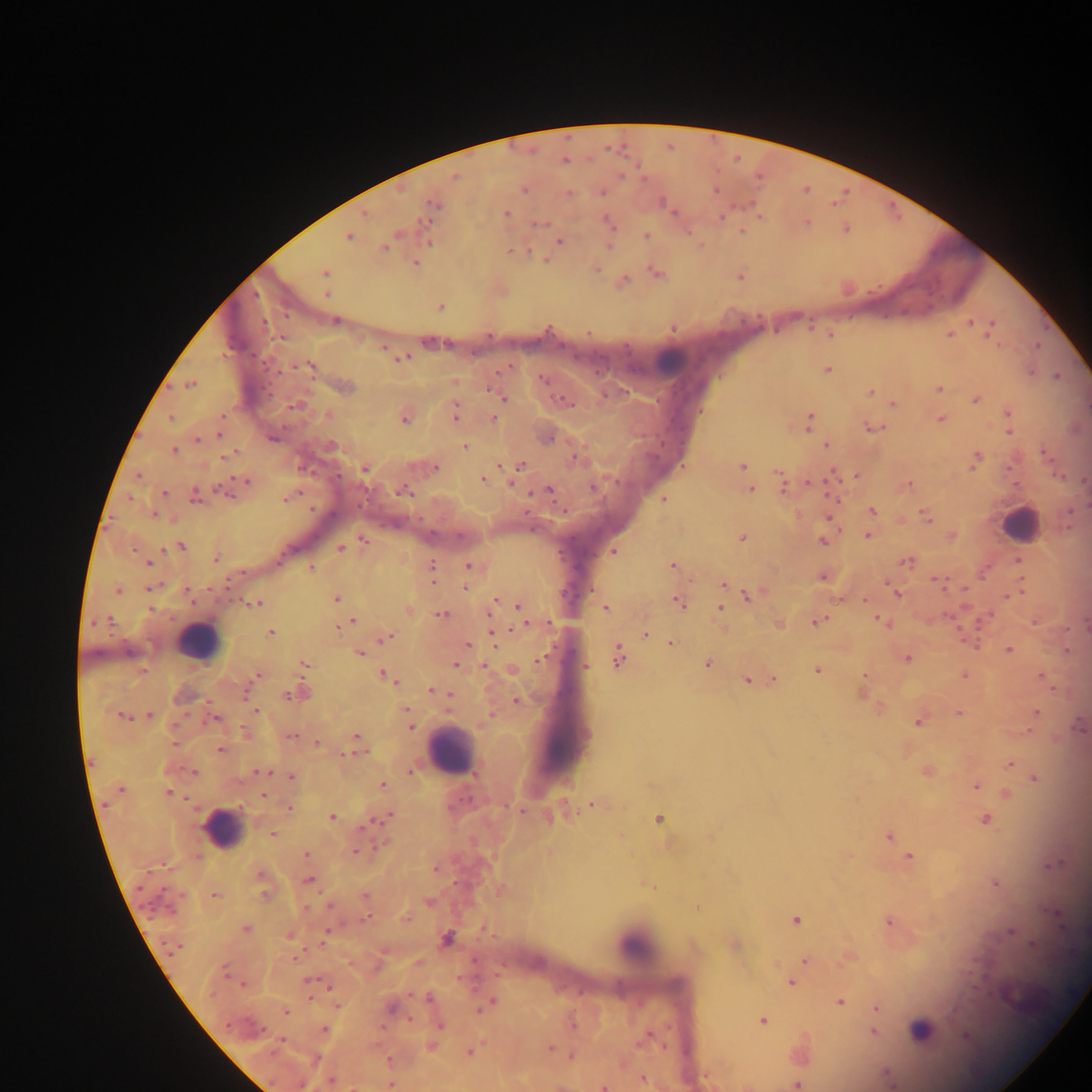
{
  "field_of_view": "single",
  "capture": "mobile-phone photograph through a microscope",
  "image_size": "1092×1092 pixels",
  "leukocyte_locations": "approximate centers as {x, y} in pixels: {671, 359}, {1018, 523}, {197, 640}, {451, 751}, {222, 829}, {635, 944}, {920, 1027}",
  "country": "Ghana",
  "preparation": "thick blood film",
  "malaria_parasite_locations": "approximate centers as {x, y} in pixels: {564, 161}, {455, 177}, {524, 190}, {716, 190}, {569, 192}, {603, 192}, {433, 205}, {671, 210}, {507, 212}, {607, 219}, {540, 224}, {742, 231}, {349, 236}, {646, 236}, {559, 241}, {429, 242}, {609, 246}, {384, 248}, {510, 251}, {545, 259}, {415, 263}, {597, 268}, {324, 273}, {658, 273}, {625, 280}, {326, 294}, {440, 306}, {336, 321}, {972, 322}, {989, 332}, {830, 334}, {949, 334}, {383, 347}, {403, 359}, {309, 367}, {827, 369}, {1057, 376}, {543, 379}, {191, 384}, {346, 386}, {490, 387}, {939, 389}, {870, 392}, {497, 395}, {504, 399}, {975, 399}, {566, 402}, {893, 404}, {296, 405}, {1007, 412}, {456, 413}, {222, 415}, {327, 415}, {170, 418}, {404, 418}, {493, 418}, {941, 419}, {810, 420}, {873, 428}, {1009, 431}, {218, 436}, {272, 438}, {550, 439}, {197, 440}, {332, 445}, {826, 445}, {464, 446}, {173, 450}, {1045, 453}, {230, 454}, {574, 459}, {976, 459}, {521, 465}, {742, 466}, {435, 468}, {365, 469}, {857, 476}, {483, 479}, {246, 480}, {908, 484}, {594, 487}, {783, 488}, {750, 489}, {221, 490}, {549, 490}, {403, 491}, {164, 493}, {195, 495}, {287, 498}, {663, 499}, {873, 511}, {926, 516}, {829, 517}, {867, 536}, {742, 538}, {364, 540}, {823, 541}, {181, 547}, {341, 548}, {614, 552}, {283, 554}, {216, 558}, {1019, 561}, {907, 562}, {147, 563}, {468, 566}, {673, 566}, {311, 567}, {431, 567}, {823, 577}, {938, 582}, {724, 584}, {148, 588}, {466, 588}, {117, 589}, {187, 590}, {897, 594}, {748, 595}, {336, 599}, {495, 600}, {865, 600}, {255, 603}, {678, 603}, {492, 606}, {518, 607}, {605, 608}, {720, 608}, {151, 609}, {408, 610}, {441, 614}, {489, 614}, {109, 620}, {353, 621}, {818, 622}, {882, 622}, {547, 623}, {339, 626}, {270, 633}, {646, 635}, {386, 637}, {493, 637}, {671, 643}, {468, 644}, {973, 645}, {1009, 649}, {360, 655}, {618, 657}, {906, 658}, {540, 660}, {304, 664}, {455, 664}, {708, 664}, {586, 666}, {484, 667}, {142, 670}, {818, 671}, {384, 674}, {257, 675}, {865, 676}, {964, 676}, {1042, 677}, {389, 678}, {774, 680}, {747, 681}, {432, 690}, {448, 694}, {287, 695}, {295, 695}, {516, 701}, {407, 709}, {256, 711}, {1036, 712}, {959, 714}, {149, 715}, {123, 716}, {491, 716}, {214, 719}, {918, 723}, {410, 727}, {244, 730}, {290, 736}, {357, 737}, {318, 743}, {175, 744}, {220, 750}, {350, 755}, {1010, 763}, {260, 771}, {193, 772}, {410, 772}, {927, 772}, {291, 777}, {1035, 778}, {383, 785}, {976, 786}, {121, 790}, {169, 792}, {263, 796}, {592, 804}, {289, 808}, {519, 811}, {387, 817}, {332, 818}, {378, 819}, {659, 819}, {985, 819}, {273, 834}, {890, 836}, {356, 852}, {306, 854}, {910, 857}, {1054, 865}, {436, 869}, {262, 874}, {309, 880}, {995, 883}, {264, 893}, {214, 894}, {364, 895}, {428, 901}, {330, 906}, {306, 908}, {698, 908}, {1057, 915}, {405, 917}, {366, 919}, {795, 920}, {889, 922}, {246, 929}, {1010, 933}, {291, 936}, {324, 938}, {446, 938}, {176, 949}, {296, 957}, {805, 961}, {225, 971}, {309, 981}, {791, 983}, {242, 984}, {329, 987}, {428, 998}, {490, 1003}, {840, 1003}, {483, 1006}, {391, 1008}, {877, 1009}, {286, 1012}, {410, 1020}, {763, 1021}, {228, 1025}, {439, 1025}, {324, 1029}, {873, 1032}, {965, 1036}, {281, 1040}, {550, 1048}, {470, 1052}, {572, 1056}, {389, 1060}, {643, 1079}, {330, 1082}, {390, 1084}, {796, 1084}, {354, 1087}, {603, 1087}"
}